Identify the parasite.
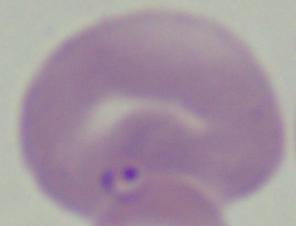
This is Babesia.

modality = micrograph
magnification = 1000x